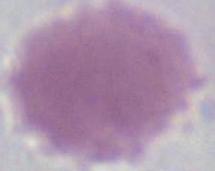
1000x magnification. An erythrocyte is seen. Photomicrograph.